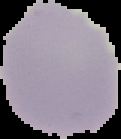
image type = cell region segmented out of the field of view; surrounding area masked to black
preparation = thin blood film
result = no Plasmodium parasites seen
image size = 121×139 pixels